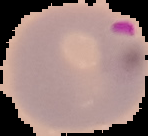
From a thin blood smear. The area outside the segmented cell region is set to black. Image is 148×136 pixels. Malaria status: parasitized.